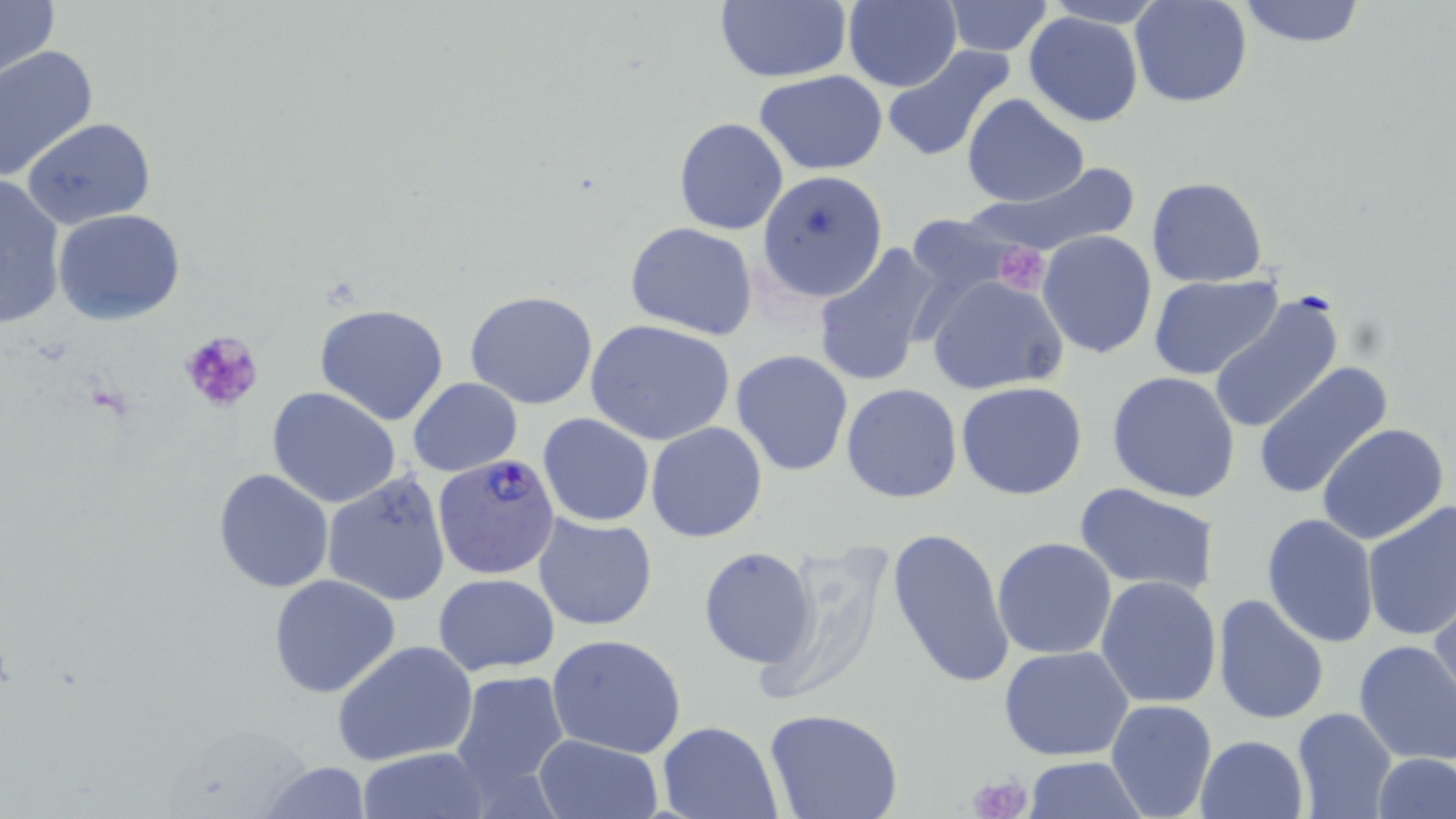

Summary:
  - Coordinate format: approximate bounding boxes as [x1, y1, x2, y2] in pixels
  - Uninfected red blood cell locations: [0, 0, 58, 85], [943, 0, 1054, 56], [1236, 0, 1369, 49], [713, 1, 853, 84], [1128, 1, 1253, 109], [842, 2, 961, 90], [1024, 11, 1145, 126], [0, 44, 98, 182], [883, 44, 1017, 162], [755, 69, 888, 174], [962, 93, 1088, 208], [24, 117, 156, 229], [674, 117, 788, 235], [977, 159, 1141, 259], [759, 170, 892, 307], [0, 174, 69, 329], [1146, 176, 1269, 288], [52, 209, 187, 326], [902, 213, 1021, 301], [625, 221, 758, 339], [1037, 230, 1158, 358], [811, 243, 940, 387], [923, 274, 1068, 395], [1150, 275, 1282, 381], [1208, 290, 1344, 438], [465, 291, 599, 410], [316, 302, 450, 426], [586, 319, 737, 445], [732, 349, 854, 478], [1253, 363, 1392, 498], [1106, 371, 1241, 502], [409, 377, 522, 476], [956, 382, 1088, 501], [842, 383, 962, 503], [267, 387, 402, 510], [538, 413, 653, 527], [645, 421, 767, 542], [1317, 421, 1450, 546], [212, 467, 336, 593], [323, 472, 453, 605], [1075, 484, 1219, 597], [1362, 501, 1456, 641], [1262, 512, 1379, 647], [533, 515, 658, 630], [885, 524, 1014, 690], [991, 537, 1118, 660], [699, 547, 818, 668], [267, 574, 402, 698], [433, 574, 559, 674], [1096, 576, 1222, 707], [1210, 593, 1329, 727], [1428, 593, 1456, 718], [546, 633, 689, 758], [334, 639, 478, 766], [1354, 639, 1456, 766], [998, 646, 1135, 762], [447, 668, 571, 803], [1105, 699, 1217, 819], [1291, 707, 1397, 819], [764, 710, 904, 819], [657, 720, 782, 818], [1195, 734, 1308, 819], [532, 735, 662, 819], [357, 748, 488, 818], [1375, 754, 1456, 818], [1024, 757, 1147, 817], [256, 762, 372, 818]
  - Platelet locations: [993, 240, 1051, 292], [181, 330, 263, 408], [969, 773, 1033, 819]
  - Plasmodium falciparum-infected red blood cell locations: [432, 452, 562, 580]
  - Slide-level diagnosis: Plasmodium falciparum
  - Preparation: thin blood film
  - Image size: 1456×819 pixels
  - Magnification: 1000x
  - Modality: optical microscopy
  - Stain: May-Grünwald-Giemsa
  - Field of view: single